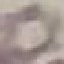

{
  "malaria_status": "uninfected",
  "capture": "smartphone through the microscope eyepiece",
  "preparation": "thin smear",
  "stain": "Giemsa",
  "image_type": "automatically extracted cell patch, resized to 64 × 64 pixels"
}